Locate every blood parasite and identify its species.
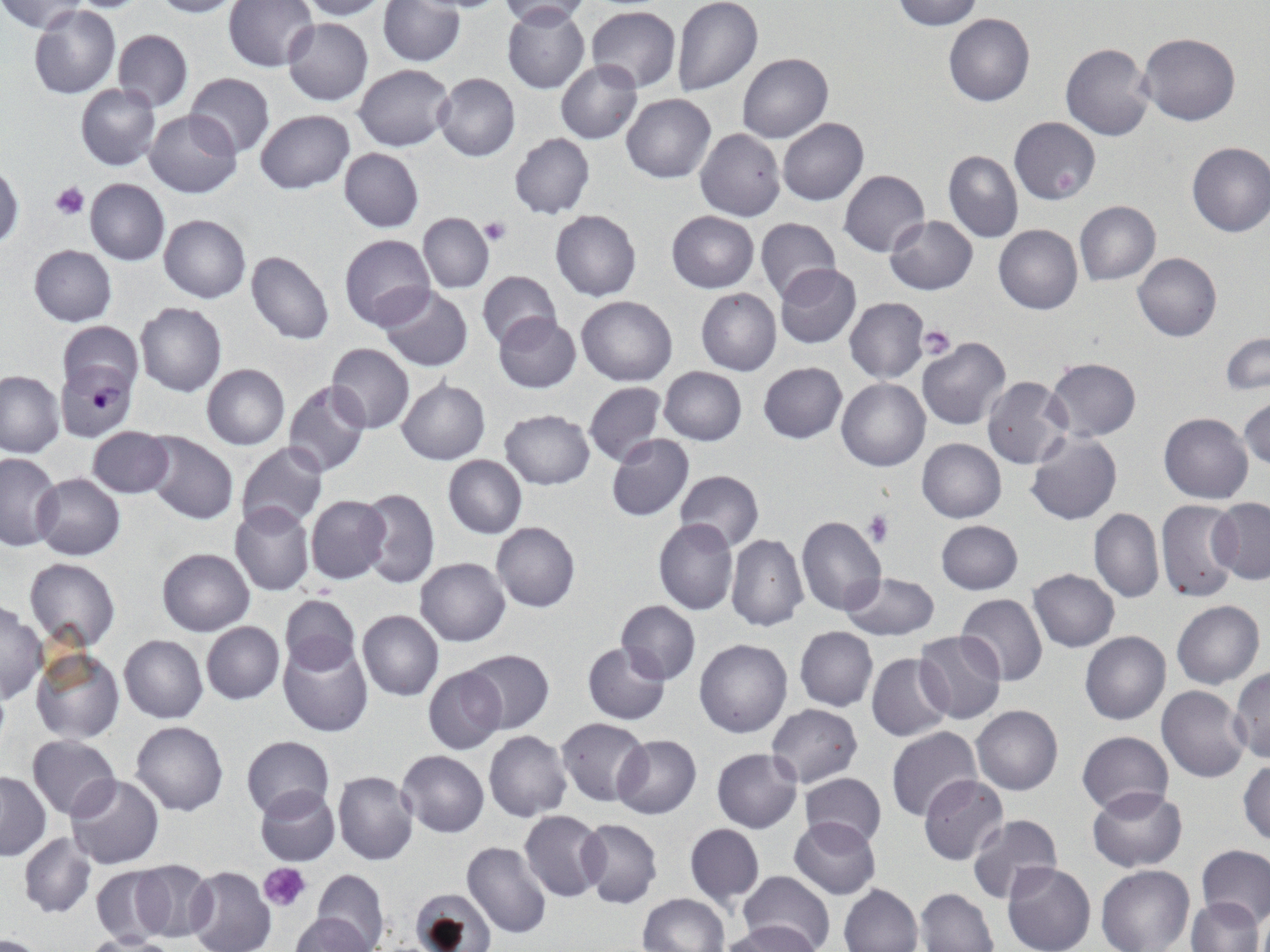
Approximate bounding boxes as (x1, y1, x2, y2) in pixels.
Plasmodium falciparum-infected red blood cells: (56, 360, 136, 441).
No Plasmodium ovale, Plasmodium malariae, Plasmodium vivax, Babesia divergens, or Trypanosoma brucei observed.

Uninfected red blood cell locations: (0, 0, 85, 34), (149, 0, 246, 18), (223, 0, 319, 72), (294, 0, 392, 20), (499, 0, 598, 25), (672, 0, 763, 97), (892, 0, 983, 30), (377, 1, 463, 67), (28, 5, 121, 98), (502, 5, 590, 94), (586, 5, 680, 91), (944, 13, 1035, 106), (283, 16, 374, 105), (113, 29, 193, 111), (1138, 32, 1241, 126), (1059, 42, 1153, 140), (738, 53, 833, 143), (556, 59, 642, 144), (354, 63, 454, 150), (434, 72, 521, 161), (185, 73, 275, 158), (75, 83, 160, 170), (621, 93, 716, 183), (145, 109, 242, 198), (255, 110, 355, 194), (778, 117, 869, 206), (1009, 117, 1101, 204), (695, 128, 785, 221), (509, 133, 594, 219), (1185, 142, 1270, 238), (339, 147, 424, 231), (943, 149, 1022, 242), (0, 162, 23, 250), (838, 170, 929, 256), (83, 179, 170, 263), (1075, 200, 1161, 285), (551, 209, 641, 301), (666, 211, 758, 292), (158, 213, 250, 303), (417, 213, 494, 292), (756, 215, 841, 305), (884, 215, 978, 294), (993, 223, 1082, 314), (339, 233, 436, 331), (29, 245, 116, 326), (246, 251, 334, 344), (1133, 253, 1221, 341), (773, 264, 862, 349), (477, 270, 561, 351), (376, 285, 473, 372), (696, 288, 781, 376), (576, 295, 677, 385), (844, 298, 929, 383), (135, 301, 227, 397), (493, 313, 581, 393), (58, 321, 142, 396), (1221, 331, 1270, 395), (916, 337, 1012, 431), (325, 343, 415, 433), (1045, 356, 1141, 441), (758, 362, 848, 444), (200, 364, 289, 449), (658, 366, 747, 445), (0, 370, 64, 457), (981, 376, 1072, 470), (836, 378, 930, 472), (396, 379, 490, 464), (282, 380, 370, 477), (583, 382, 667, 466), (1239, 396, 1269, 474), (499, 408, 595, 489), (1159, 412, 1253, 503), (87, 427, 173, 498), (145, 431, 239, 524), (1026, 431, 1123, 527), (606, 433, 694, 520), (917, 438, 1006, 522), (236, 442, 328, 531), (0, 452, 62, 550), (443, 455, 527, 538), (674, 470, 765, 551), (33, 472, 126, 559), (357, 487, 439, 589), (305, 495, 391, 584), (1208, 497, 1270, 584), (1155, 499, 1242, 605), (229, 502, 316, 597), (1089, 508, 1164, 604), (795, 514, 887, 616), (654, 518, 738, 615), (936, 520, 1023, 594), (491, 522, 580, 612), (725, 534, 808, 631), (156, 548, 254, 636), (415, 557, 511, 646), (23, 558, 121, 653), (1028, 568, 1120, 652), (840, 571, 940, 641), (280, 593, 361, 675), (957, 594, 1048, 684), (615, 599, 701, 684), (1171, 599, 1264, 688), (0, 602, 45, 703), (357, 610, 443, 701), (200, 621, 284, 704), (795, 627, 877, 712), (1079, 630, 1171, 725), (914, 631, 1006, 725), (119, 635, 207, 722), (124, 637, 214, 812), (279, 637, 372, 736), (695, 638, 792, 738), (576, 641, 661, 805), (582, 641, 670, 724), (30, 649, 124, 743), (461, 649, 554, 735), (866, 652, 953, 741), (422, 666, 507, 754), (1230, 668, 1269, 763), (1157, 685, 1250, 782), (766, 704, 862, 787), (972, 705, 1063, 795), (557, 718, 650, 805), (131, 720, 228, 815), (886, 726, 981, 821), (484, 730, 573, 821), (1076, 730, 1173, 815), (241, 734, 334, 817), (612, 734, 701, 819), (27, 735, 120, 820), (711, 748, 802, 832), (397, 750, 488, 836), (1238, 759, 1269, 847), (0, 770, 50, 859), (333, 770, 419, 865), (798, 772, 887, 847), (64, 774, 167, 869), (918, 775, 1007, 864), (255, 785, 340, 865), (1087, 785, 1189, 872), (520, 810, 606, 902), (967, 814, 1064, 905), (789, 816, 881, 900), (576, 818, 663, 908), (684, 822, 764, 907), (812, 823, 900, 937), (19, 833, 96, 918), (463, 842, 551, 939), (1197, 845, 1270, 928), (130, 860, 217, 942), (1002, 862, 1096, 952), (1096, 865, 1195, 952), (91, 866, 171, 943), (187, 866, 277, 952), (311, 868, 388, 950), (738, 869, 835, 952), (838, 883, 922, 952), (409, 887, 500, 952), (916, 888, 999, 952), (639, 892, 729, 952), (1187, 898, 1263, 952), (294, 907, 382, 952), (1255, 907, 1270, 952), (722, 921, 823, 952), (0, 934, 51, 952), (81, 934, 182, 951). Platelet locations: (50, 181, 90, 221), (480, 218, 511, 247), (917, 325, 957, 359), (864, 509, 894, 547), (262, 864, 309, 911). Slide-level diagnosis: Plasmodium falciparum. One field of a larger specimen. Image is 1270×952 pixels. May-Grünwald-Giemsa stain. 1000x magnification. Thin blood smear. Light microscopy.